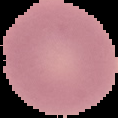
result: no Plasmodium parasites detected
image_size: 118×118 pixels
image_type: cell region segmented out of the field of view; surrounding area masked to black
preparation: thin blood smear